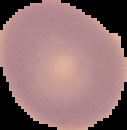
From a thin blood smear. Image is 127×130 pixels. Result: no malaria parasites detected. The area outside the segmented cell region is set to black.